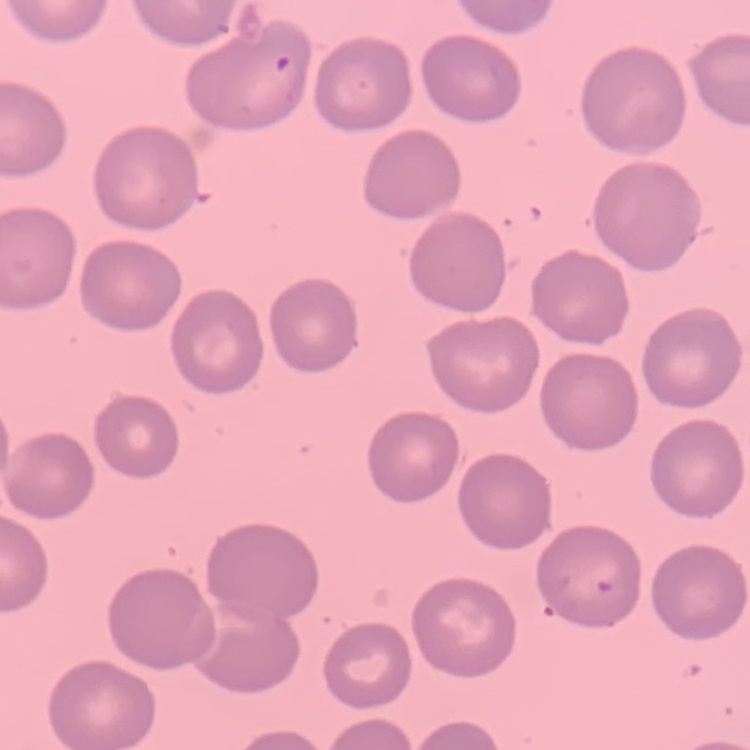 The erythrocytes exhibit no rouleaux formation. Stained with either Field's or Giemsa. One tile cut from a larger photomicrograph. Thin peripheral smear.